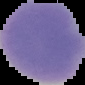 From a thin blood film. Image is 85×85 pixels. Segmented cell region on a black background. Result: no Plasmodium parasites detected.